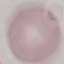 Result: negative for malaria parasites. Photographed with a smartphone camera at the microscope eyepiece. Thin blood film. Giemsa-stained preparation. Cell patch, automatically extracted from a larger field of view and resized to 64 × 64 pixels.